Comment on the morphology of the red blood cells.
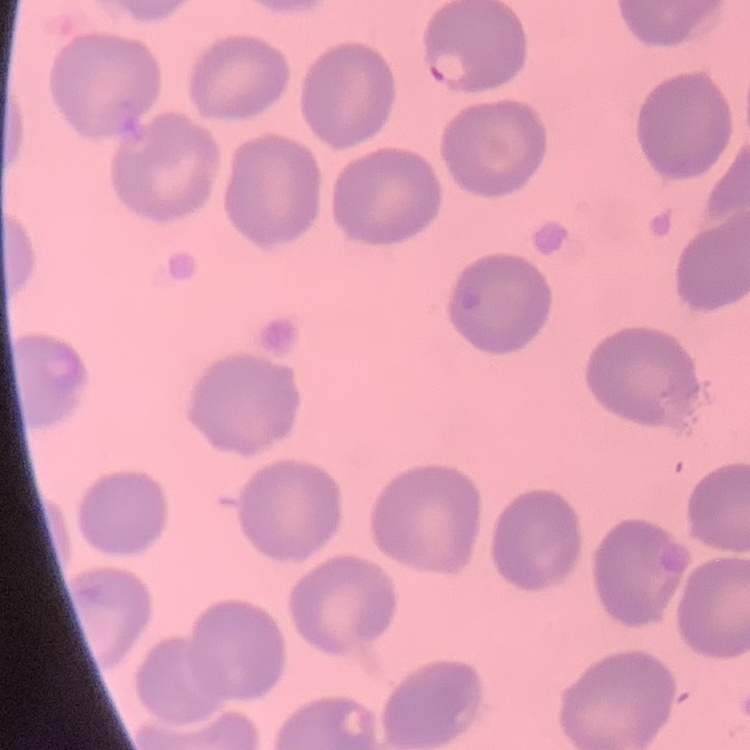
They show no rouleaux formation.

Thin blood smear. Square crop of a larger photomicrograph. Stained with either Field's or Giemsa.